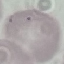

Malaria status: uninfected. Thin smear of blood. Giemsa-stained preparation. Cell patch, automatically extracted from a larger field of view and resized to 64 × 64 pixels. Acquired by smartphone through the microscope eyepiece.